State which parasite is depicted.
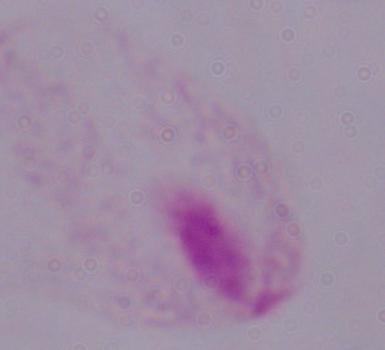
This is a trichomonad.

Summary:
  - Magnification: 1000x
  - Modality: micrograph